Locate and identify every blood parasite.
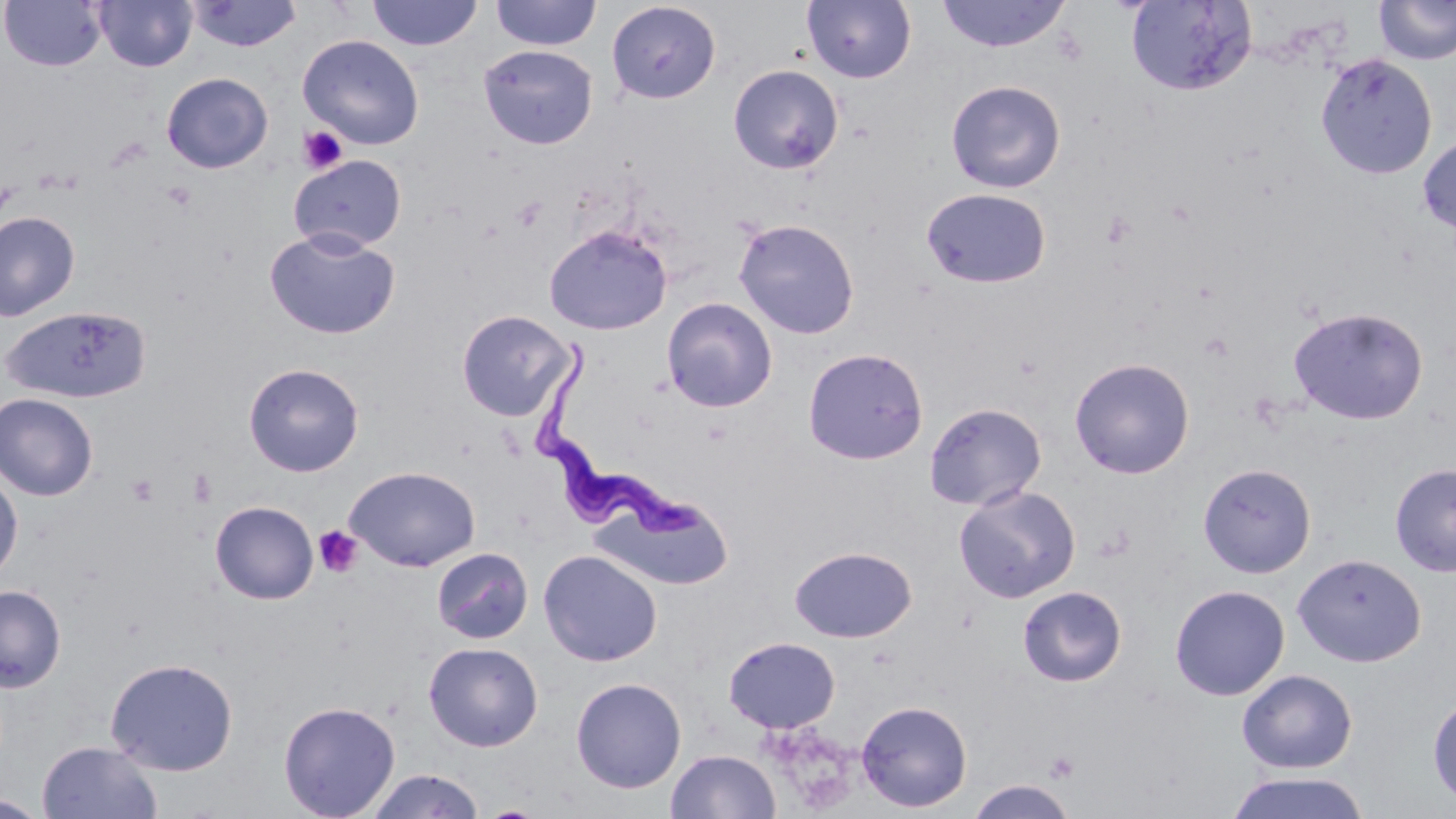
Approximate bounding boxes as [x1, y1, x2, y2] in pixels.
Trypanosoma brucei: [528, 345, 709, 546].
No Plasmodium falciparum, Plasmodium ovale, Plasmodium malariae, Plasmodium vivax, or Babesia divergens observed.

slide-level diagnosis = Trypanosoma brucei
platelet locations = approximate bounding boxes as [x1, y1, x2, y2] in pixels: [298, 125, 348, 174], [511, 196, 547, 231], [1100, 210, 1138, 248], [1199, 332, 1235, 362], [187, 468, 216, 508], [125, 473, 161, 506], [313, 526, 363, 579], [1044, 751, 1080, 783]
stain = May-Grünwald-Giemsa
modality = optical microscopy
magnification = 1000x
image size = 1456×819 pixels
preparation = thin blood smear
uninfected red blood cell locations = approximate bounding boxes as [x1, y1, x2, y2] in pixels: [94, 0, 197, 72], [490, 0, 602, 51], [802, 0, 916, 84], [935, 0, 1072, 53], [1125, 0, 1257, 96], [1374, 0, 1456, 66], [1, 1, 106, 71], [186, 1, 302, 52], [367, 1, 482, 51], [606, 2, 721, 104], [298, 34, 425, 150], [478, 44, 598, 149], [1315, 53, 1437, 178], [728, 64, 845, 174], [161, 72, 273, 173], [945, 79, 1066, 193], [1417, 135, 1456, 235], [288, 154, 407, 254], [921, 187, 1052, 289], [0, 211, 80, 321], [733, 218, 860, 339], [544, 224, 672, 335], [264, 227, 401, 340], [662, 297, 778, 413], [2, 305, 151, 404], [1288, 306, 1428, 425], [456, 310, 574, 421], [803, 347, 929, 465], [1069, 357, 1195, 479], [243, 362, 364, 477], [0, 393, 99, 500], [924, 402, 1047, 511], [1389, 462, 1456, 577], [1198, 463, 1316, 579], [345, 465, 481, 571], [0, 469, 23, 582], [954, 484, 1081, 603], [594, 491, 733, 589], [210, 501, 319, 604], [790, 546, 916, 642], [432, 547, 533, 643], [538, 550, 662, 667], [1292, 553, 1426, 667], [1170, 584, 1289, 701], [0, 585, 66, 692], [1017, 585, 1127, 687], [723, 636, 840, 733], [423, 641, 543, 751], [105, 657, 238, 775], [1236, 669, 1358, 774], [570, 677, 687, 793], [1427, 694, 1456, 809], [278, 700, 400, 818], [855, 700, 972, 812], [36, 741, 162, 819], [666, 749, 781, 819], [364, 769, 486, 818], [1225, 770, 1372, 819], [966, 779, 1077, 819]
field of view = one of a larger specimen